Classify this cell by malaria status.
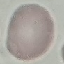
It is uninfected.

Summary:
  - Preparation: thin blood film
  - Stain: Giemsa
  - Image type: cell patch, automatically extracted from a larger field of view and resized to 64 × 64 pixels
  - Capture: smartphone camera at the microscope eyepiece